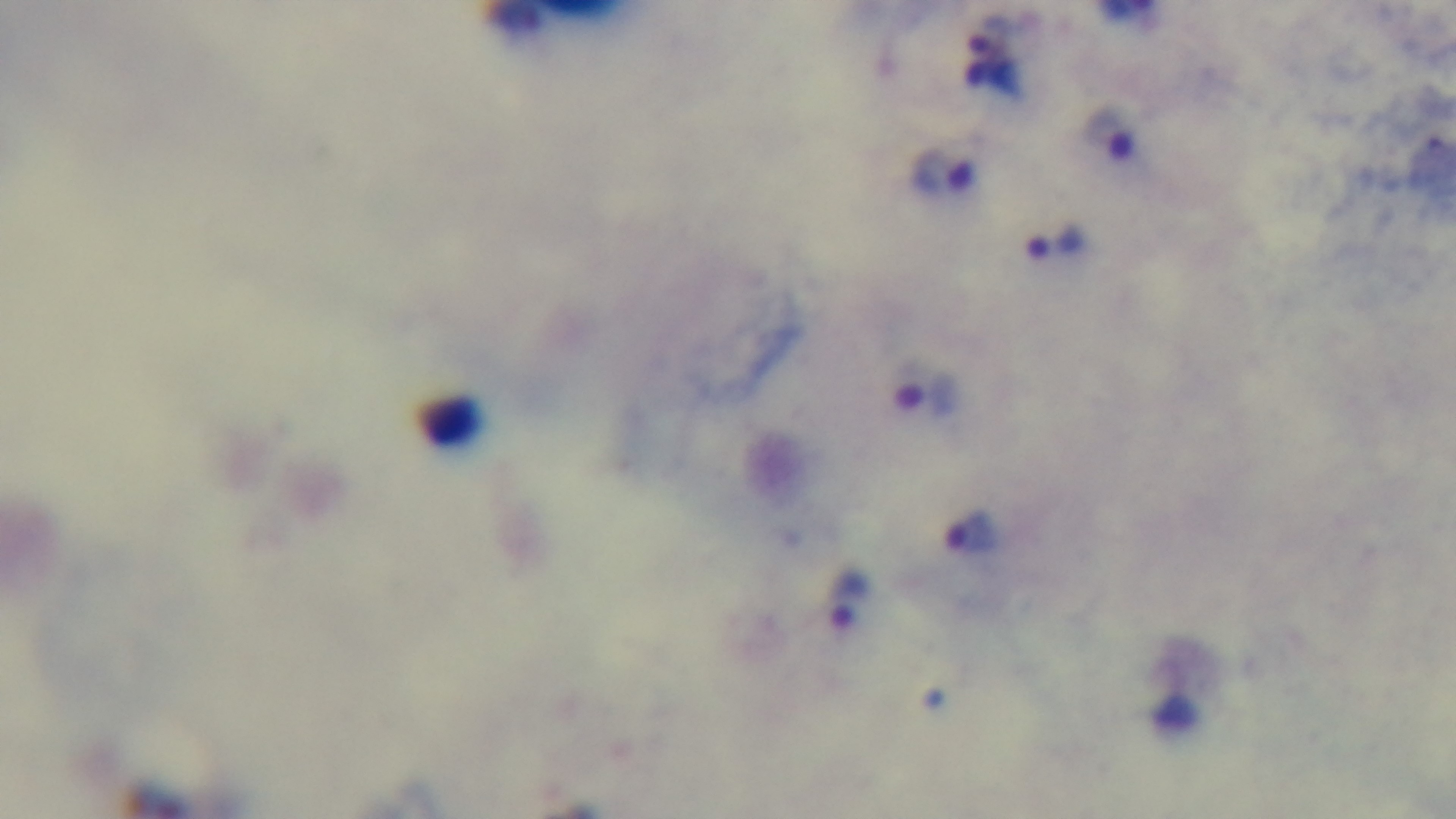 Giemsa-stained. Preparation: thick blood film. Malaria status: infected. One field from the slide. 100x oil-immersion objective. Captured with a mounted 4K digital camera. Photomicrograph.